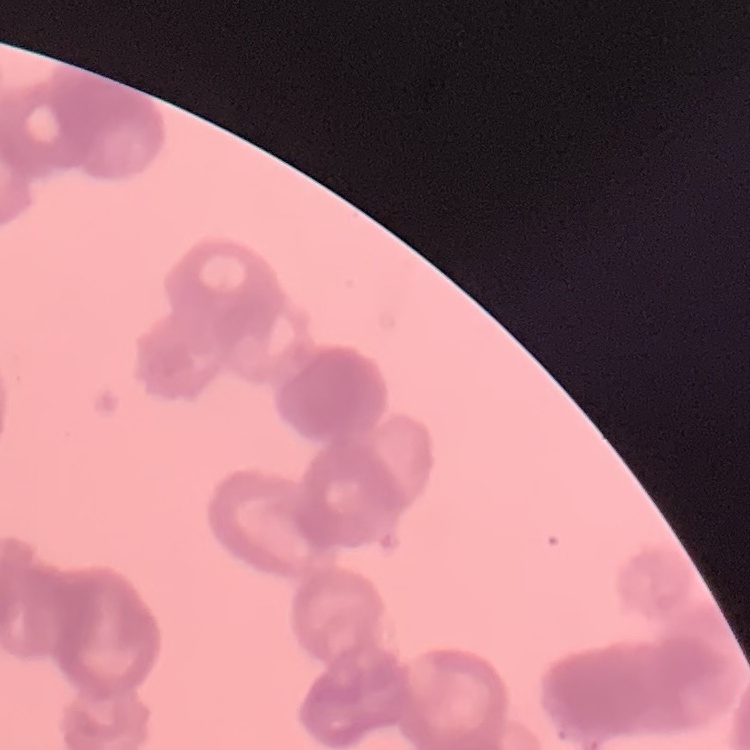
Summary:
  - Erythrocyte morphology: rouleaux formation
  - Stain: Field's or Giemsa
  - Image type: one tile cut from a larger photomicrograph
  - Preparation: thin blood film